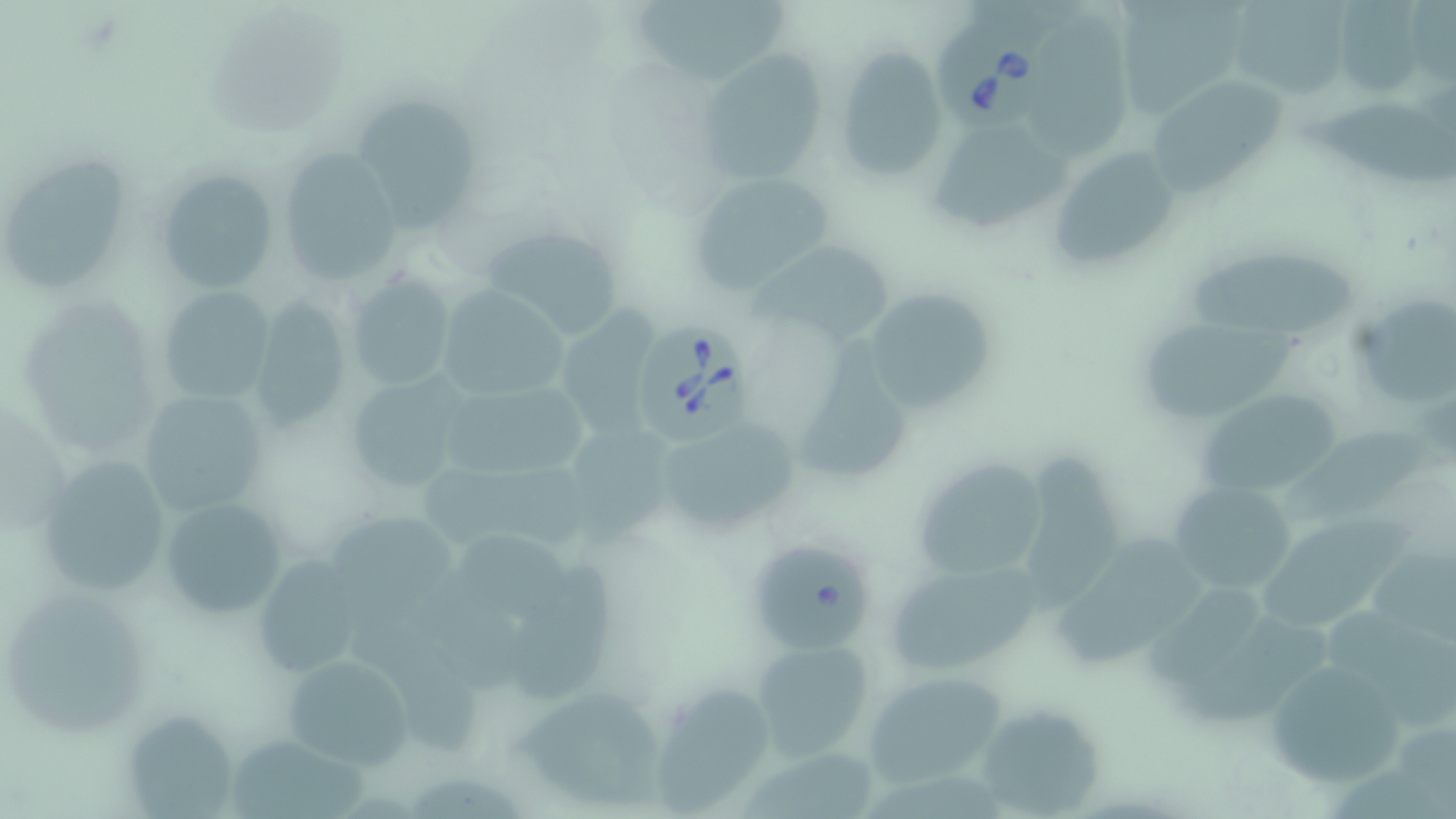
Summary:
  - Coordinate format: approximate bounding boxes as (x1,y1)-(x2,y2) corner pairs in pixels
  - Uninfected red blood cell locations: (1236,0)-(1353,99), (628,1)-(791,91), (1338,1)-(1422,96), (1030,9)-(1136,166), (832,46)-(950,184), (695,50)-(827,185), (1152,83)-(1284,194), (352,92)-(483,234), (1306,99)-(1456,189), (931,123)-(1073,239), (276,145)-(404,289), (1049,145)-(1181,272), (4,154)-(132,290), (151,167)-(279,295), (688,171)-(836,294), (480,224)-(627,340), (761,237)-(898,342), (1189,251)-(1357,335), (347,274)-(459,390), (154,287)-(275,405), (435,287)-(566,400), (863,287)-(995,415), (1359,298)-(1454,409), (248,299)-(358,434), (561,302)-(651,438), (1142,323)-(1312,428), (798,335)-(915,484), (340,373)-(474,497), (446,376)-(591,476), (1196,383)-(1345,499), (136,389)-(270,519), (660,424)-(802,525), (1289,424)-(1439,522), (34,453)-(172,596), (1023,453)-(1119,620), (910,455)-(1052,583), (418,460)-(587,554), (1166,480)-(1298,599), (158,495)-(292,621), (1263,513)-(1419,633), (458,532)-(582,627), (755,544)-(879,659), (1055,545)-(1208,676), (1368,551)-(1456,646), (511,555)-(618,699), (250,557)-(371,675), (892,568)-(1040,677), (1149,583)-(1263,691), (4,596)-(147,739), (1321,606)-(1456,732), (751,640)-(875,758), (1259,649)-(1408,791), (278,650)-(416,770), (862,671)-(1008,789), (653,683)-(775,814), (519,686)-(666,806), (981,707)-(1103,814), (128,715)-(234,819), (232,733)-(366,819)
  - Babesia divergens-infected red blood cell locations: (933,16)-(1057,134), (632,320)-(758,451)
  - Slide-level diagnosis: Babesia divergens
  - Magnification: 1000x
  - Modality: light microscopy
  - Field of view: single
  - Image size: 1456×819 pixels
  - Preparation: thin blood film
  - Stain: May-Grünwald-Giemsa